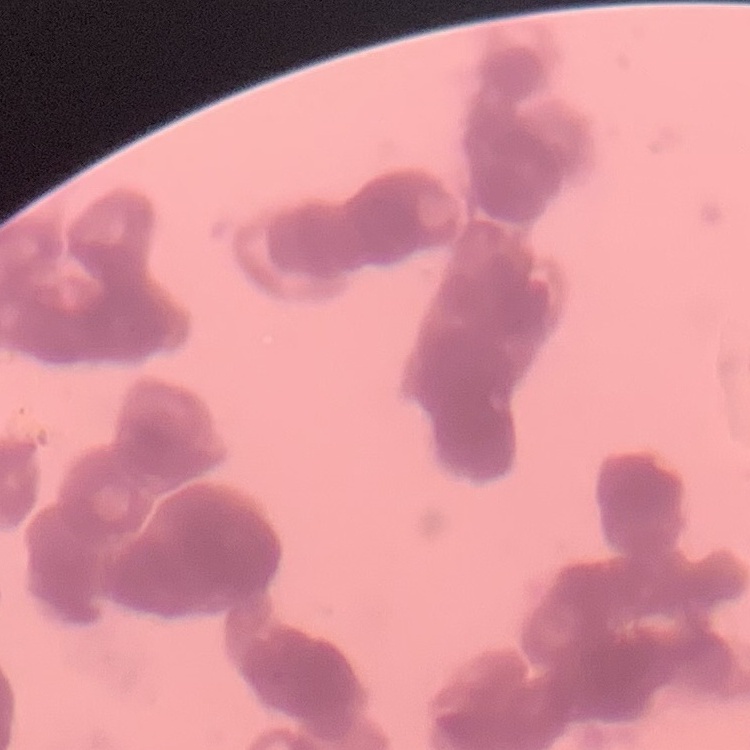 The erythrocytes show rouleaux formation. Thin blood smear. Square crop of a larger photomicrograph. Stained with either Field's or Giemsa.